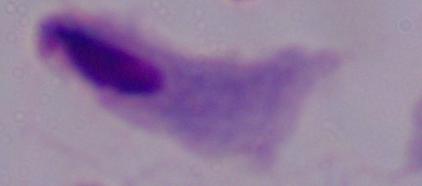
modality: micrograph
magnification: 1000x
identification: trichomonad